Assess this cell for malaria.
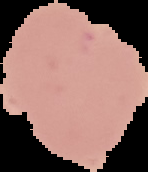
Uninfected.

Summary:
  - Image type: cell region segmented out of the field of view; surrounding area masked to black
  - Image size: 148×172 pixels
  - Preparation: thin blood smear